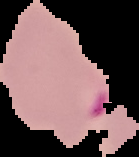

Summary:
  - Image type: cell region segmented out of the field of view; surrounding area masked to black
  - Preparation: thin blood smear
  - Image size: 139×157 pixels
  - Malaria status: parasitized